Report the malaria status of this cell.
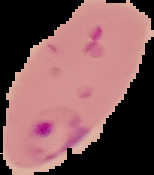

Parasitized.

Summary:
  - Preparation: thin blood film
  - Image size: 154×175 pixels
  - Image type: cell region segmented out of the field of view; surrounding area masked to black